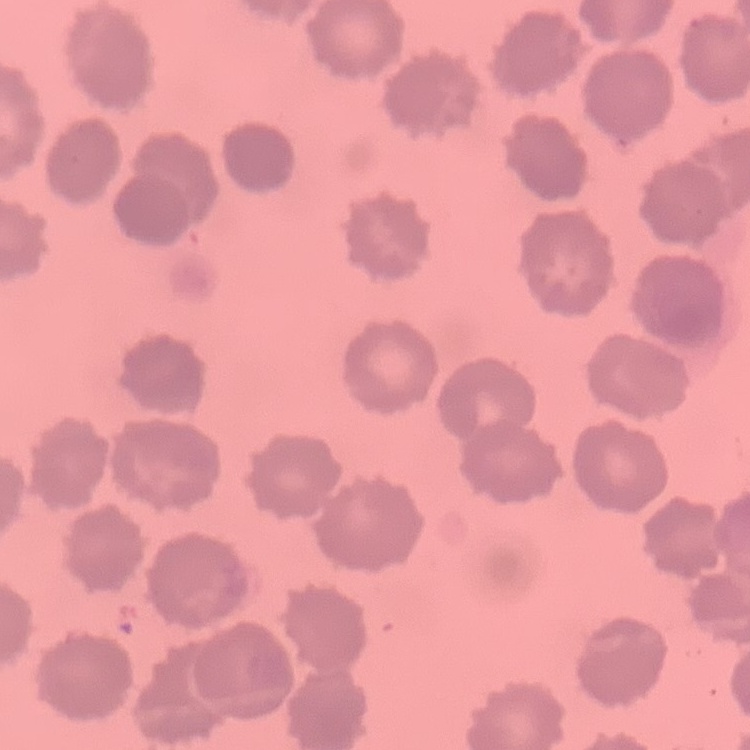
red_blood_cell_morphology: no rouleaux formation
stain: Field's or Giemsa
preparation: thin blood film
image_type: one tile cut from a larger photomicrograph